State which cell type is depicted.
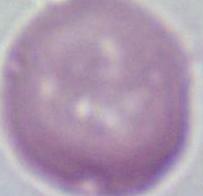
An erythrocyte.

Micrograph. Captured at 1000x magnification.